Evaluate for malaria.
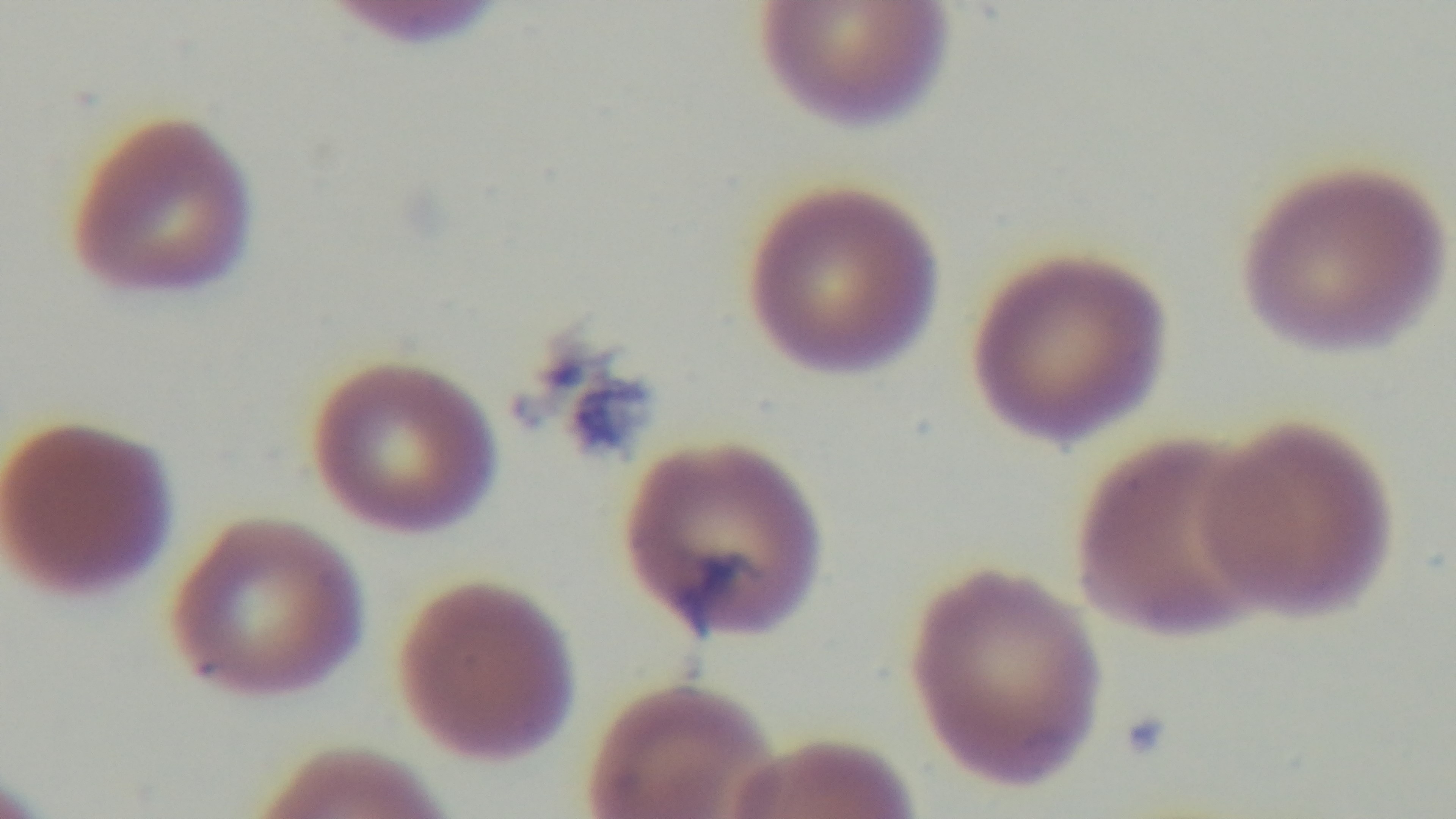

Positive.

Summary:
  - Preparation: thin blood film
  - Objective: 100x oil immersion
  - Modality: light microscopy
  - Field of view: one from the slide
  - Stain: Giemsa
  - Capture: mounted 4K digital camera